Assess the morphology of the red blood cells.
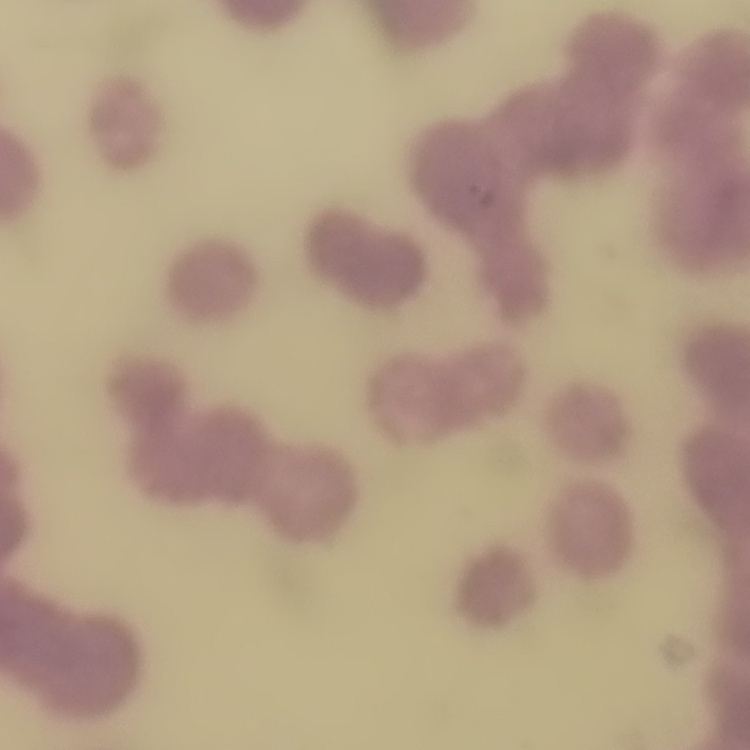

Rouleaux formation.

{
  "preparation": "thin peripheral smear",
  "stain": "Field's or Giemsa",
  "image_type": "one tile cut from a larger photomicrograph"
}